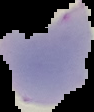
Image is 94×112 pixels. Cell region segmented out of the field of view; the surrounding area is masked to black. From a thin blood smear. Result: Plasmodium parasites identified.